Give the extent of the malaria parasites you find, grouped by life-cycle stage — ring form, trophozoite, schizont, or gametocyte.
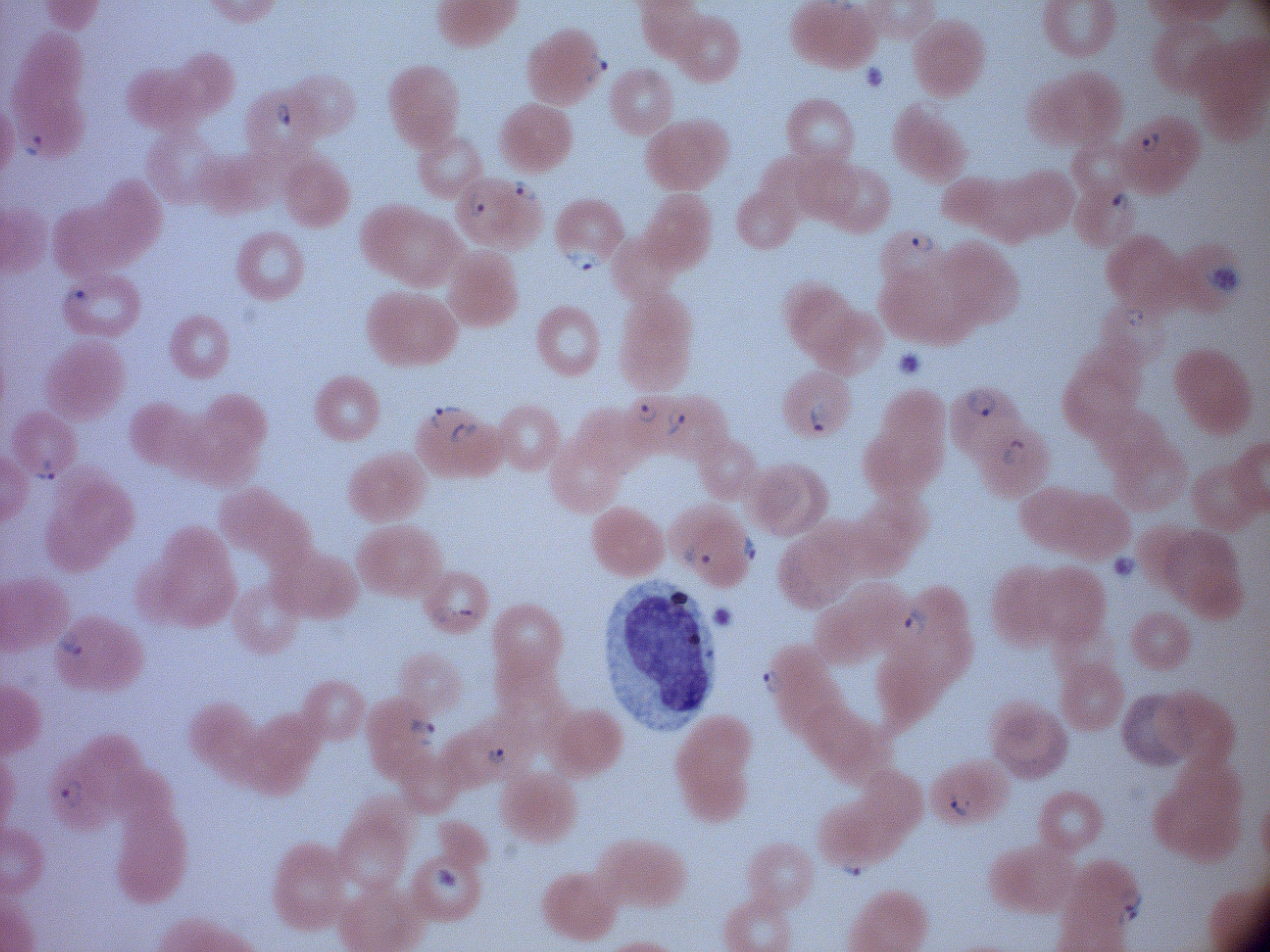
Approximate bounding boxes as named x1/y1/x2/y2 corners in pixels, from the source annotation, which is not necessarily exhaustive.
Ring forms: (x1=580, y1=48, x2=611, y2=86), (x1=269, y1=98, x2=297, y2=133), (x1=1135, y1=122, x2=1165, y2=159), (x1=14, y1=126, x2=47, y2=157), (x1=506, y1=176, x2=539, y2=204), (x1=1106, y1=183, x2=1136, y2=216), (x1=466, y1=190, x2=490, y2=220), (x1=905, y1=231, x2=935, y2=258), (x1=565, y1=242, x2=604, y2=277), (x1=57, y1=283, x2=96, y2=310), (x1=1123, y1=302, x2=1152, y2=333), (x1=964, y1=386, x2=998, y2=419), (x1=808, y1=393, x2=835, y2=437), (x1=424, y1=402, x2=461, y2=430), (x1=633, y1=403, x2=659, y2=426), (x1=660, y1=408, x2=689, y2=438), (x1=448, y1=419, x2=480, y2=448), (x1=1001, y1=434, x2=1032, y2=466), (x1=27, y1=456, x2=60, y2=489), (x1=739, y1=529, x2=763, y2=570), (x1=676, y1=539, x2=718, y2=569), (x1=431, y1=602, x2=481, y2=631), (x1=901, y1=603, x2=931, y2=643), (x1=53, y1=627, x2=85, y2=661), (x1=760, y1=665, x2=783, y2=697), (x1=404, y1=714, x2=440, y2=750), (x1=479, y1=739, x2=515, y2=771), (x1=57, y1=772, x2=88, y2=812), (x1=944, y1=787, x2=975, y2=821), (x1=837, y1=858, x2=876, y2=879), (x1=1110, y1=888, x2=1149, y2=930).

Summary:
  - Magnification: 100x
  - Image size: 1270×952 pixels
  - Preparation: thin blood smear
  - Microscope: Leica DM2000 with built-in camera
  - Field of view: single
  - Species: Plasmodium falciparum
  - Stain: Giemsa